Classify this cell by malaria status.
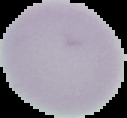

Uninfected.

preparation: thin blood smear
image_type: cell region segmented out of the field of view; surrounding area masked to black
image_size: 127×118 pixels